Comment on the morphology of the red blood cells.
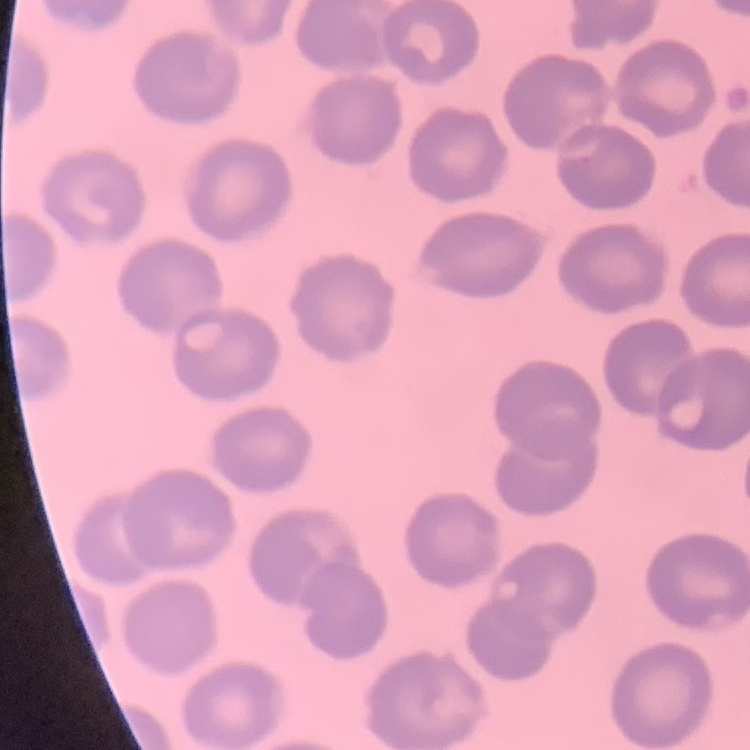
No rouleaux formation.

Summary:
  - Image type: square crop of a larger photomicrograph
  - Preparation: thin blood film
  - Stain: Field's or Giemsa